Name the cell type shown.
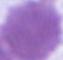

An erythrocyte.

magnification = 1000x
modality = micrograph